Outline each blood parasite and name the species.
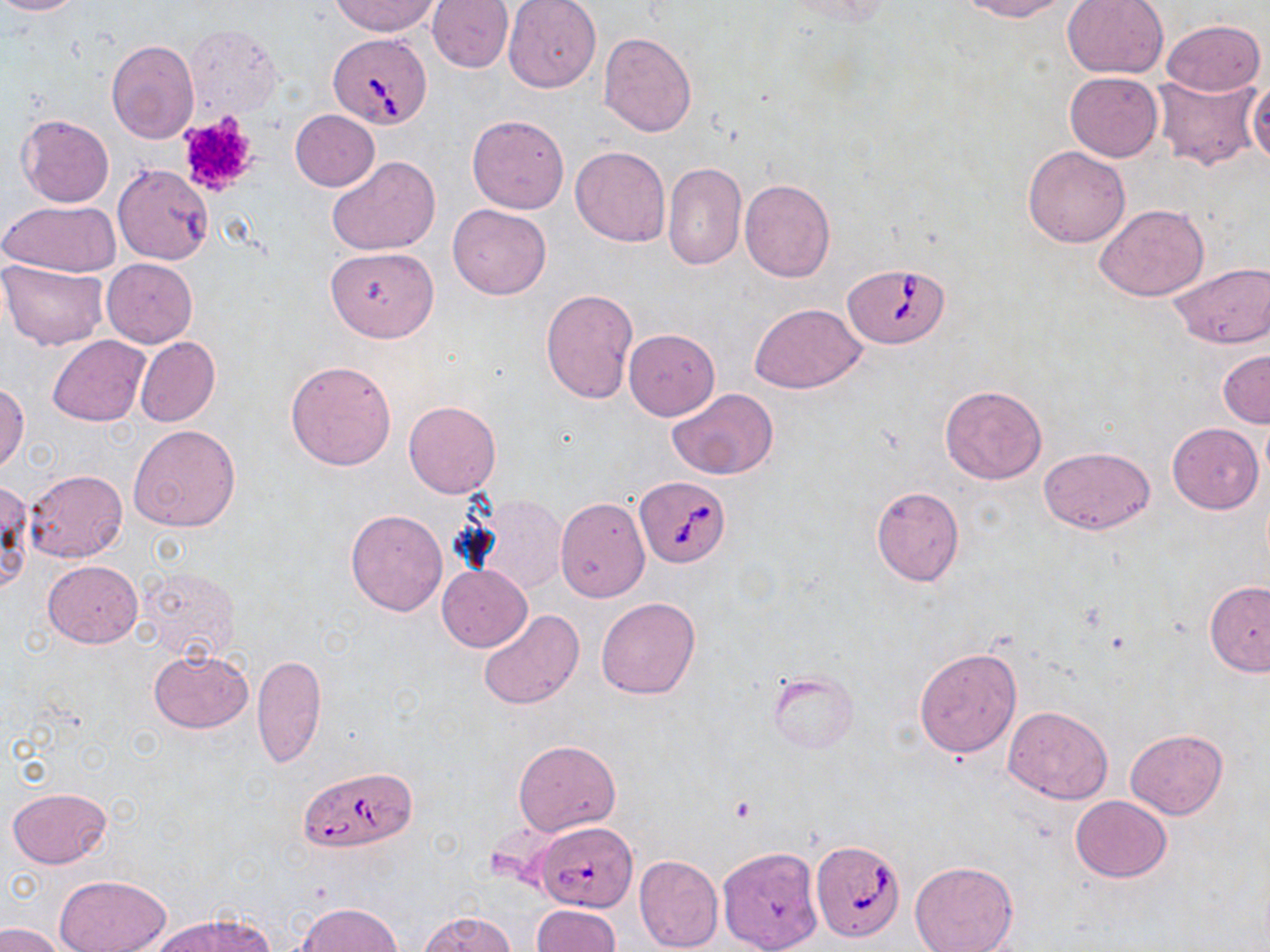
Approximate bounding boxes as named x1/y1/x2/y2 corners in pixels.
Babesia divergens-infected red blood cells: (x1=328, y1=32, x2=432, y2=128), (x1=844, y1=261, x2=952, y2=348), (x1=636, y1=475, x2=731, y2=569), (x1=298, y1=767, x2=418, y2=854), (x1=532, y1=821, x2=636, y2=912), (x1=811, y1=839, x2=905, y2=941).
No Plasmodium falciparum, Plasmodium ovale, Plasmodium malariae, Plasmodium vivax, or Trypanosoma brucei observed.

Summary:
  - Platelet locations: (x1=177, y1=112, x2=258, y2=197)
  - Uninfected red blood cell locations: (x1=0, y1=0, x2=85, y2=16), (x1=331, y1=0, x2=441, y2=36), (x1=427, y1=0, x2=513, y2=73), (x1=958, y1=0, x2=1072, y2=21), (x1=1062, y1=0, x2=1169, y2=78), (x1=502, y1=1, x2=599, y2=92), (x1=1161, y1=18, x2=1266, y2=97), (x1=184, y1=24, x2=282, y2=119), (x1=598, y1=32, x2=696, y2=137), (x1=106, y1=39, x2=199, y2=143), (x1=1065, y1=71, x2=1164, y2=161), (x1=1151, y1=74, x2=1262, y2=172), (x1=1247, y1=78, x2=1270, y2=168), (x1=289, y1=109, x2=380, y2=191), (x1=17, y1=113, x2=113, y2=208), (x1=467, y1=113, x2=570, y2=214), (x1=570, y1=145, x2=672, y2=246), (x1=1022, y1=145, x2=1132, y2=248), (x1=327, y1=155, x2=440, y2=256), (x1=662, y1=162, x2=746, y2=269), (x1=113, y1=164, x2=212, y2=265), (x1=740, y1=179, x2=835, y2=282), (x1=2, y1=200, x2=121, y2=278), (x1=448, y1=203, x2=551, y2=299), (x1=1094, y1=203, x2=1210, y2=301), (x1=325, y1=246, x2=439, y2=342), (x1=102, y1=258, x2=197, y2=347), (x1=0, y1=261, x2=109, y2=351), (x1=1168, y1=263, x2=1267, y2=348), (x1=540, y1=289, x2=638, y2=403), (x1=749, y1=303, x2=867, y2=393), (x1=623, y1=329, x2=719, y2=420), (x1=47, y1=336, x2=150, y2=425), (x1=135, y1=336, x2=220, y2=428), (x1=1218, y1=348, x2=1270, y2=429), (x1=285, y1=359, x2=397, y2=471), (x1=0, y1=382, x2=29, y2=471), (x1=940, y1=384, x2=1047, y2=484), (x1=667, y1=388, x2=778, y2=479), (x1=404, y1=401, x2=501, y2=498), (x1=1168, y1=423, x2=1263, y2=514), (x1=128, y1=424, x2=241, y2=533), (x1=1039, y1=446, x2=1155, y2=536), (x1=25, y1=469, x2=126, y2=562), (x1=0, y1=480, x2=32, y2=594), (x1=871, y1=486, x2=963, y2=586), (x1=473, y1=494, x2=568, y2=594), (x1=555, y1=496, x2=650, y2=602), (x1=345, y1=509, x2=448, y2=616), (x1=43, y1=560, x2=142, y2=646), (x1=437, y1=565, x2=531, y2=651), (x1=137, y1=566, x2=239, y2=663), (x1=1204, y1=580, x2=1270, y2=676), (x1=595, y1=596, x2=701, y2=699), (x1=478, y1=609, x2=585, y2=711), (x1=915, y1=647, x2=1022, y2=758), (x1=147, y1=650, x2=252, y2=733), (x1=252, y1=652, x2=326, y2=769), (x1=767, y1=672, x2=858, y2=753), (x1=1002, y1=706, x2=1112, y2=804), (x1=1124, y1=728, x2=1229, y2=819), (x1=513, y1=740, x2=620, y2=835), (x1=7, y1=787, x2=112, y2=868), (x1=1069, y1=796, x2=1172, y2=881), (x1=714, y1=841, x2=819, y2=948), (x1=634, y1=854, x2=722, y2=951), (x1=908, y1=860, x2=1019, y2=952), (x1=56, y1=875, x2=169, y2=952), (x1=296, y1=902, x2=400, y2=952), (x1=531, y1=904, x2=620, y2=952), (x1=420, y1=912, x2=519, y2=952), (x1=153, y1=914, x2=273, y2=952), (x1=0, y1=923, x2=65, y2=952)
  - Slide-level diagnosis: Babesia divergens
  - Image size: 1270×952 pixels
  - Stain: May-Grünwald-Giemsa
  - Magnification: 1000x
  - Preparation: thin blood film
  - Modality: light microscopy
  - Field of view: single